Name the parasite shown.
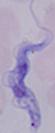

This is a trypanosome.

Summary:
  - Modality: micrograph
  - Magnification: 1000x